Describe the morphology of the red blood cells.
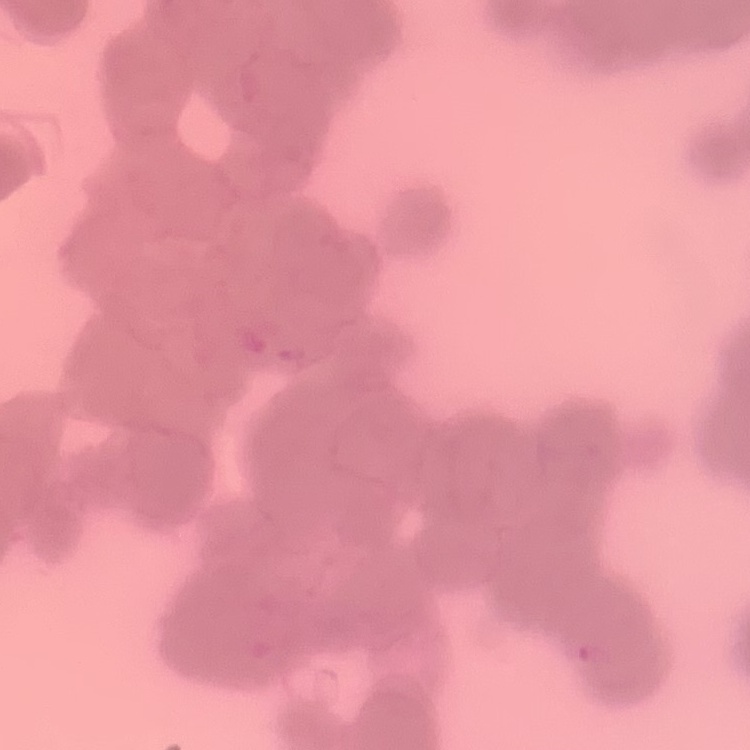

Rouleaux formation.

Summary:
  - Preparation: thin blood film
  - Stain: Field's or Giemsa
  - Image type: one tile cut from a larger photomicrograph